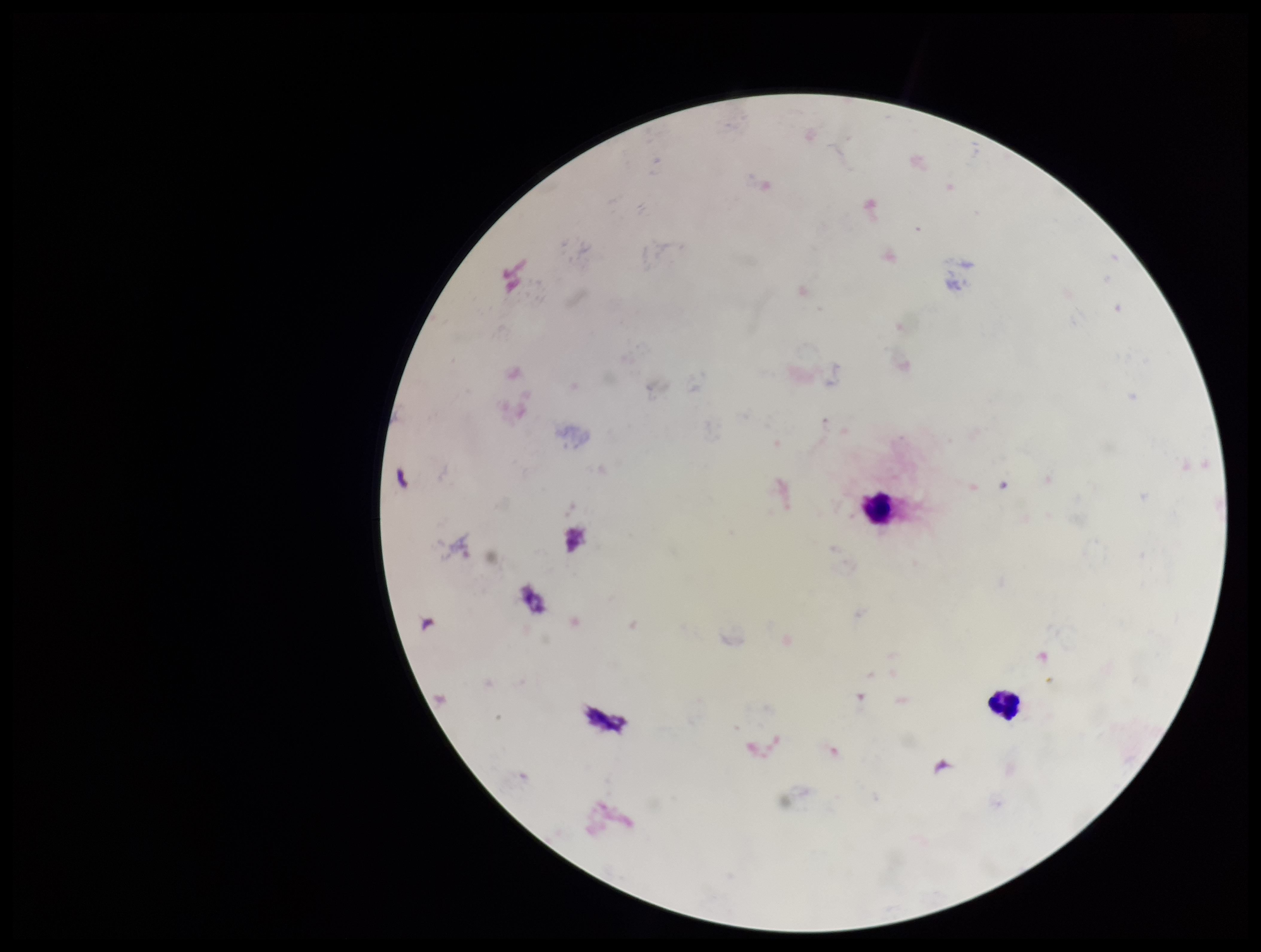
Summary:
  - Patient malaria status: negative
  - Capture: smartphone photograph through the microscope eyepiece
  - Preparation: thick blood smear
  - Field of view: one from this slide
  - Leukocyte count: 2
  - Stain: Giemsa
  - Plasmodium parasites: none identified
  - Image size: 1261×952 pixels
  - Parasite count: 0